Report the malaria status of this cell.
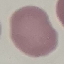

Uninfected.

capture = smartphone camera at the microscope eyepiece
stain = Giemsa
preparation = thin blood film
image type = automatically extracted cell patch, resized to 64 × 64 pixels